Describe the morphology of the red blood cells.
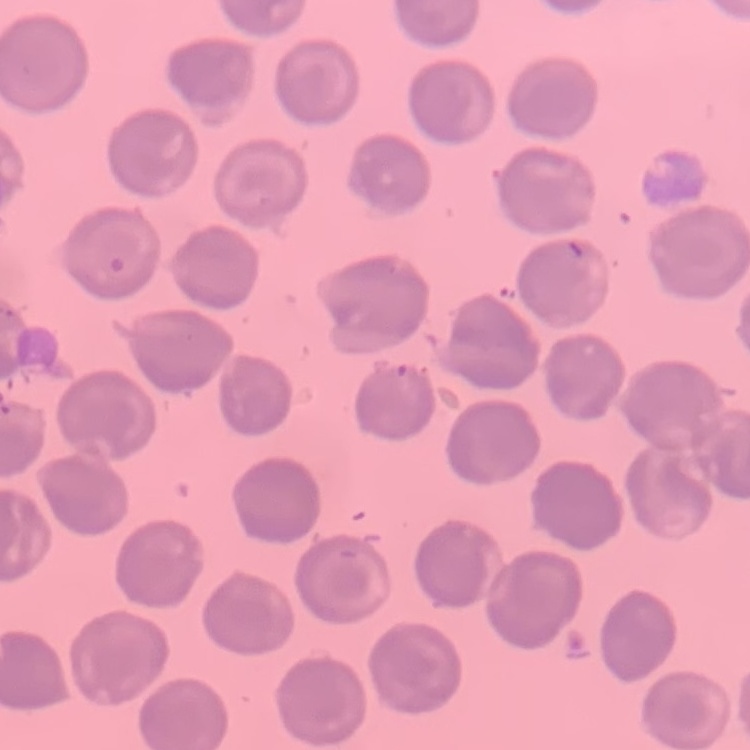

They show no rouleaux formation.

preparation: thin peripheral smear
stain: Field's or Giemsa
image_type: square crop of a larger photomicrograph